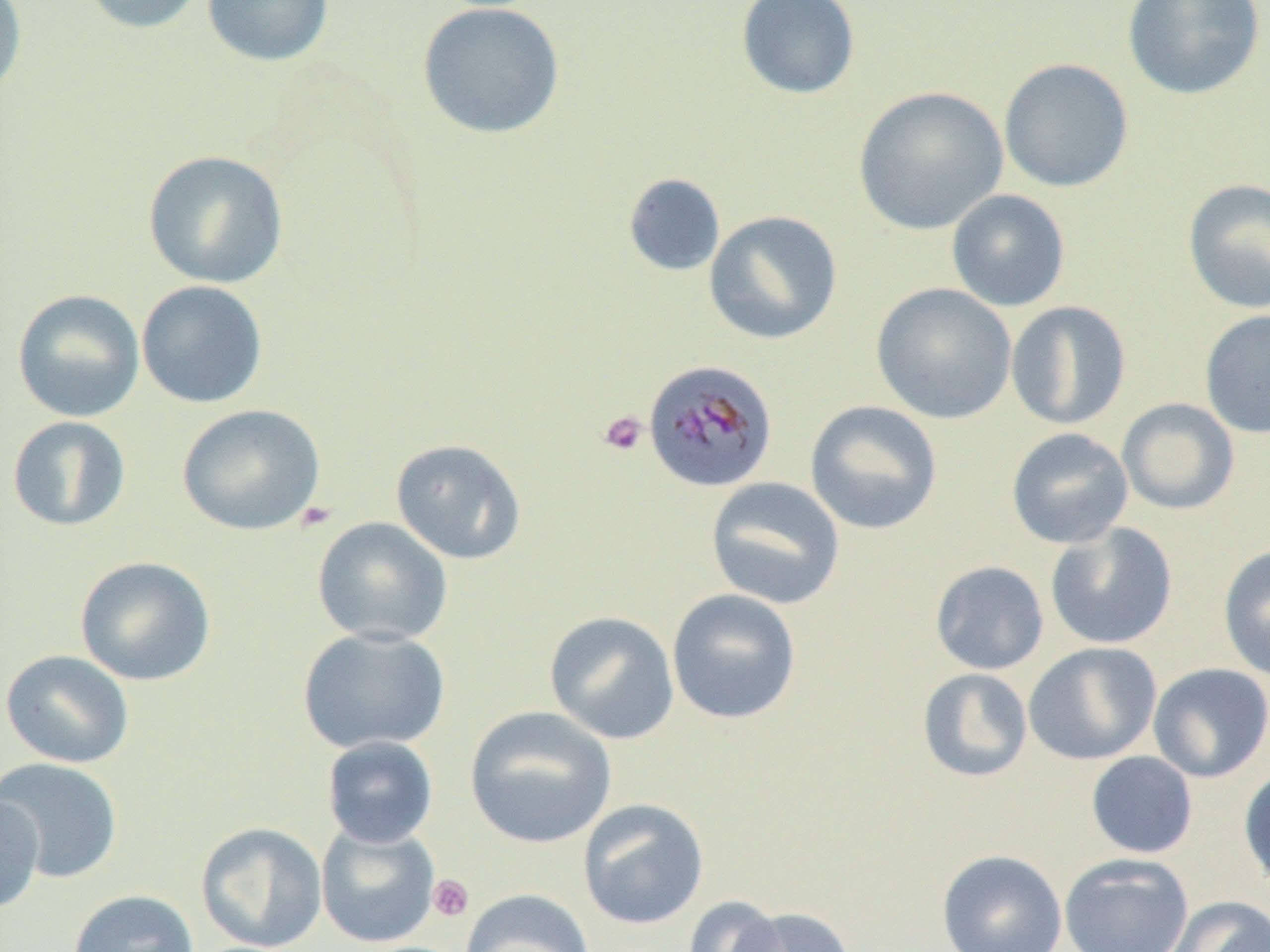
Plasmodium malariae-infected red blood cell locations = approximate bounding boxes as named x1/y1/x2/y2 corners in pixels: (x1=643, y1=358, x2=778, y2=492)
slide-level diagnosis = Plasmodium malariae
magnification = 1000x
uninfected red blood cell locations = approximate bounding boxes as named x1/y1/x2/y2 corners in pixels: (x1=0, y1=0, x2=28, y2=101), (x1=79, y1=0, x2=207, y2=35), (x1=201, y1=0, x2=335, y2=67), (x1=735, y1=0, x2=860, y2=99), (x1=1121, y1=0, x2=1266, y2=100), (x1=417, y1=2, x2=566, y2=140), (x1=998, y1=58, x2=1134, y2=193), (x1=853, y1=86, x2=1008, y2=235), (x1=142, y1=149, x2=289, y2=289), (x1=623, y1=173, x2=726, y2=277), (x1=1182, y1=178, x2=1270, y2=314), (x1=946, y1=189, x2=1071, y2=312), (x1=703, y1=210, x2=842, y2=345), (x1=136, y1=280, x2=269, y2=409), (x1=871, y1=282, x2=1017, y2=424), (x1=12, y1=289, x2=146, y2=422), (x1=1005, y1=300, x2=1131, y2=430), (x1=1199, y1=308, x2=1270, y2=439), (x1=1117, y1=398, x2=1240, y2=515), (x1=804, y1=400, x2=943, y2=535), (x1=176, y1=403, x2=326, y2=536), (x1=6, y1=416, x2=131, y2=531), (x1=1006, y1=428, x2=1134, y2=549), (x1=390, y1=438, x2=527, y2=565), (x1=705, y1=477, x2=846, y2=610), (x1=311, y1=517, x2=454, y2=647), (x1=1045, y1=522, x2=1178, y2=650), (x1=1218, y1=544, x2=1270, y2=682), (x1=74, y1=556, x2=216, y2=687), (x1=930, y1=560, x2=1049, y2=675), (x1=666, y1=589, x2=802, y2=725), (x1=543, y1=611, x2=679, y2=744), (x1=297, y1=626, x2=451, y2=754), (x1=1023, y1=642, x2=1161, y2=765), (x1=1, y1=650, x2=135, y2=769), (x1=1148, y1=662, x2=1270, y2=783), (x1=917, y1=667, x2=1033, y2=782), (x1=464, y1=706, x2=617, y2=848), (x1=321, y1=736, x2=439, y2=848), (x1=1086, y1=751, x2=1198, y2=859), (x1=0, y1=757, x2=123, y2=884), (x1=1238, y1=765, x2=1270, y2=891), (x1=0, y1=792, x2=45, y2=914), (x1=577, y1=799, x2=709, y2=930), (x1=195, y1=821, x2=328, y2=952), (x1=316, y1=822, x2=441, y2=948), (x1=936, y1=849, x2=1068, y2=952), (x1=1059, y1=853, x2=1194, y2=952), (x1=67, y1=889, x2=199, y2=952), (x1=460, y1=889, x2=594, y2=952), (x1=682, y1=895, x2=788, y2=952), (x1=1166, y1=895, x2=1270, y2=952), (x1=731, y1=906, x2=856, y2=952)
modality = light microscopy
platelet locations = approximate bounding boxes as named x1/y1/x2/y2 corners in pixels: (x1=598, y1=411, x2=648, y2=457), (x1=427, y1=874, x2=474, y2=922)
field of view = single
image size = 1270×952 pixels
preparation = thin blood smear